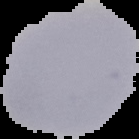 The area outside the segmented cell region is set to black. Image is 139×139 pixels. From a thin blood film. Malaria status: uninfected.